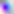
{
  "magnification": "400x",
  "identification": "Toxoplasma gondii",
  "modality": "micrograph"
}